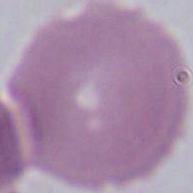

magnification = 1000x
identification = red blood cell
modality = photomicrograph